Classify this cell by malaria status.
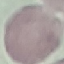

Uninfected.

capture: smartphone through the microscope eyepiece
preparation: thin blood film
stain: Giemsa
image_type: automatically extracted cell patch, resized to 64 × 64 pixels